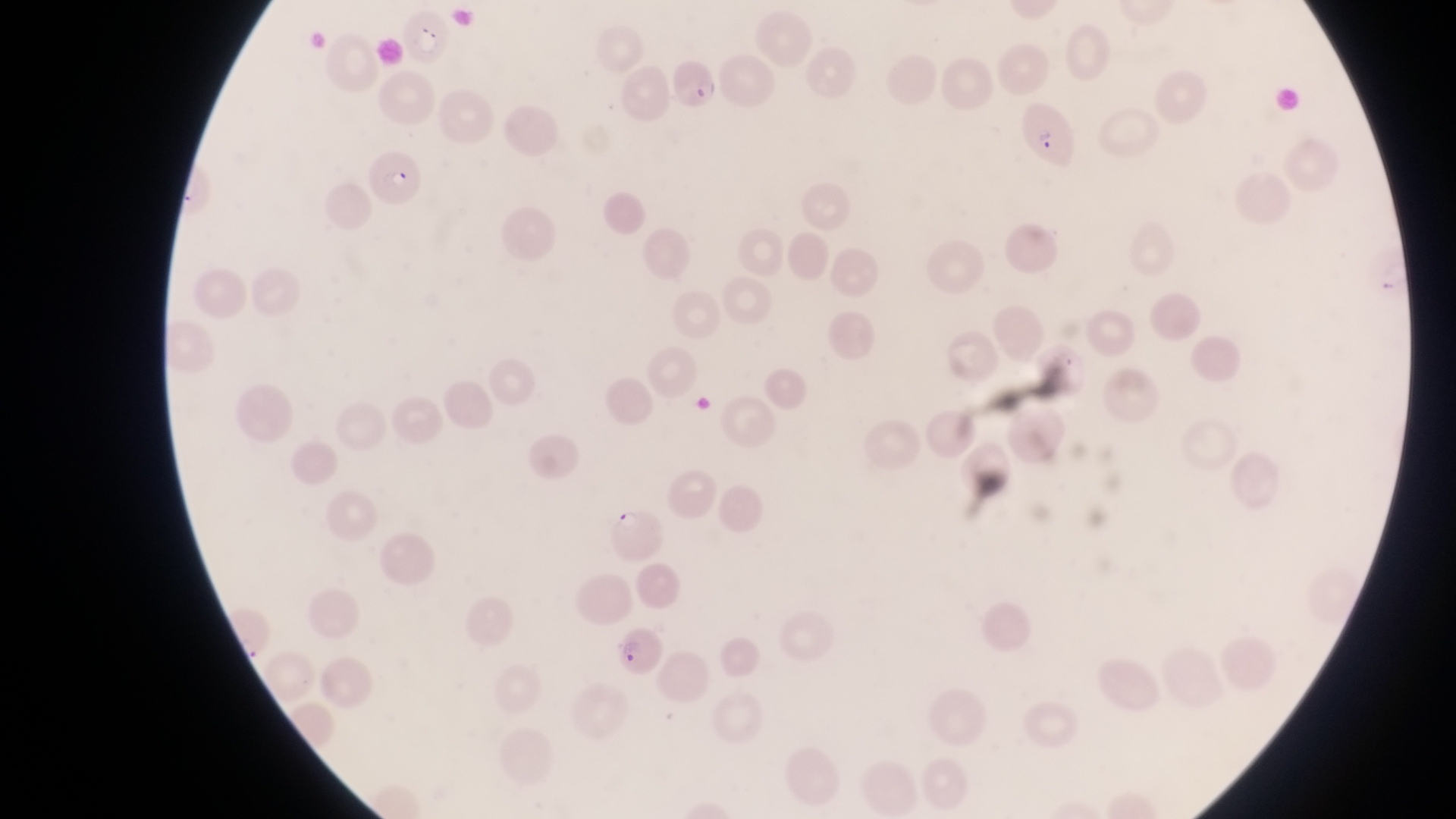
image_size: 1456×819 pixels
artifact_platelet_like_body_stain_precipitate_or_debris_locations: 'approximate bounding boxes as left top right bottom in pixels: 692 388 719 424'
capture: smartphone photograph through the eyepiece of an Olympus CX-23 microscope
parasitised_red_blood_cell_locations: 'approximate bounding boxes as left top right bottom in pixels: 399 5 449 66; 668 58 720 114; 1017 99 1081 170; 366 151 430 212; 608 500 664 563; 616 631 662 677'
field_of_view: single
magnification: 1000x
country: Uganda
preparation: thin blood film